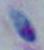
{
  "identification": "Toxoplasma gondii",
  "magnification": "1000x",
  "modality": "photomicrograph"
}